Report the malaria status of this cell.
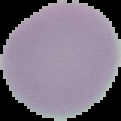

It is uninfected.

Image is 121×121 pixels. The area outside the segmented cell region is set to black. From a thin blood smear.